Name the blood parasite species.
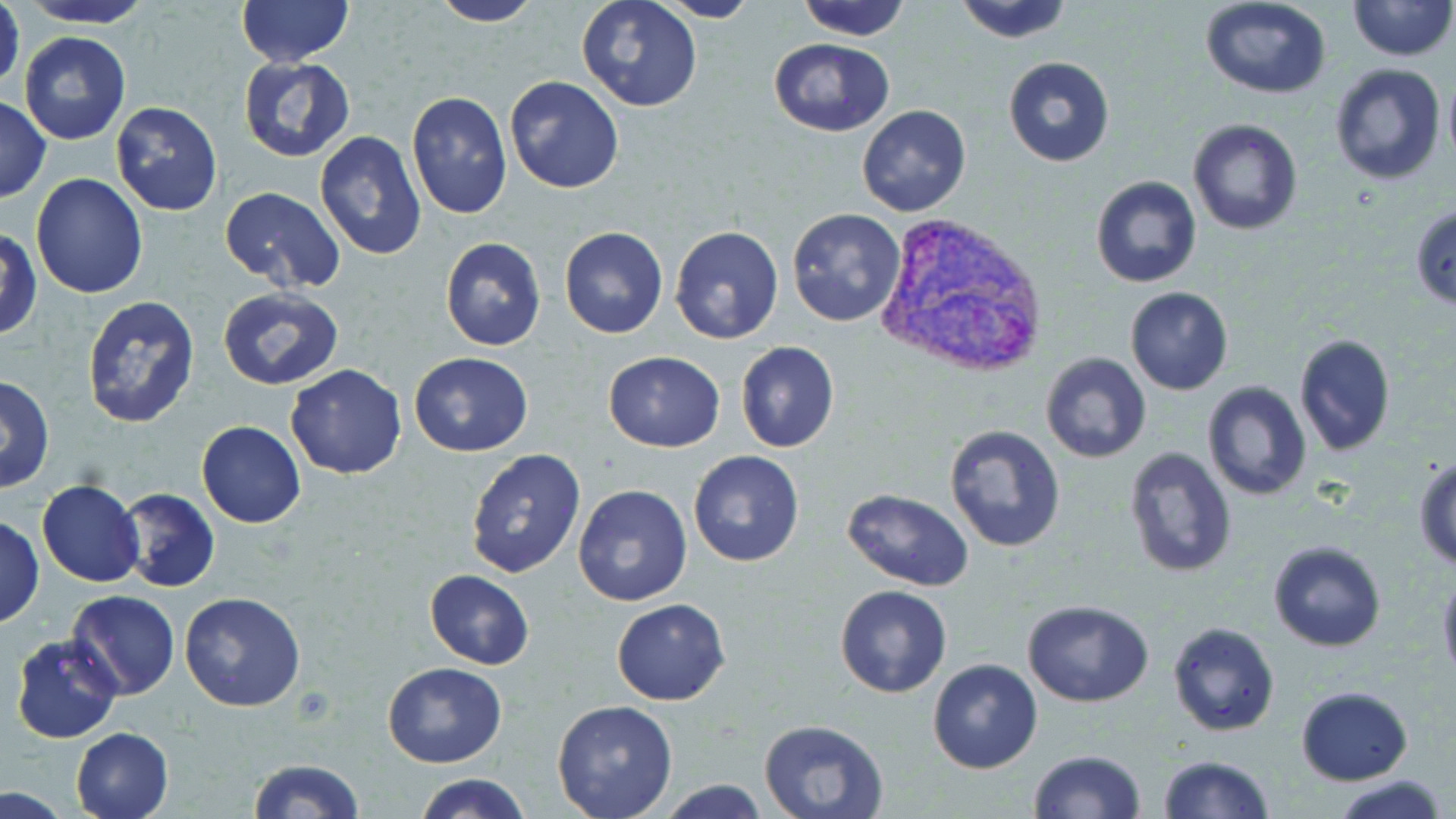
Plasmodium vivax.

Approximate bounding boxes as named x1/y1/x2/y2 corners in pixels. Uninfected red blood cell locations: (x1=18, y1=0, x2=157, y2=29), (x1=234, y1=0, x2=357, y2=67), (x1=576, y1=0, x2=704, y2=112), (x1=795, y1=0, x2=911, y2=42), (x1=952, y1=0, x2=1074, y2=44), (x1=1198, y1=0, x2=1333, y2=100), (x1=1348, y1=0, x2=1452, y2=61), (x1=1, y1=1, x2=24, y2=102), (x1=424, y1=1, x2=544, y2=27), (x1=655, y1=1, x2=762, y2=23), (x1=20, y1=31, x2=130, y2=146), (x1=768, y1=36, x2=894, y2=137), (x1=239, y1=56, x2=354, y2=162), (x1=1002, y1=57, x2=1115, y2=167), (x1=1329, y1=63, x2=1447, y2=185), (x1=1442, y1=69, x2=1456, y2=168), (x1=504, y1=74, x2=625, y2=194), (x1=406, y1=91, x2=511, y2=219), (x1=0, y1=94, x2=51, y2=203), (x1=111, y1=102, x2=222, y2=216), (x1=856, y1=104, x2=972, y2=217), (x1=1187, y1=119, x2=1303, y2=235), (x1=314, y1=131, x2=428, y2=261), (x1=31, y1=173, x2=148, y2=299), (x1=1090, y1=175, x2=1202, y2=288), (x1=218, y1=184, x2=346, y2=294), (x1=1410, y1=203, x2=1456, y2=309), (x1=787, y1=209, x2=908, y2=328), (x1=670, y1=226, x2=784, y2=344), (x1=559, y1=227, x2=668, y2=339), (x1=2, y1=230, x2=41, y2=340), (x1=440, y1=237, x2=547, y2=351), (x1=1125, y1=287, x2=1233, y2=396), (x1=219, y1=289, x2=344, y2=391), (x1=79, y1=294, x2=201, y2=431), (x1=1292, y1=333, x2=1397, y2=457), (x1=735, y1=341, x2=840, y2=453), (x1=603, y1=351, x2=725, y2=452), (x1=1040, y1=351, x2=1152, y2=464), (x1=408, y1=352, x2=533, y2=457), (x1=286, y1=364, x2=407, y2=480), (x1=0, y1=375, x2=54, y2=493), (x1=1202, y1=380, x2=1313, y2=501), (x1=196, y1=421, x2=306, y2=528), (x1=943, y1=424, x2=1068, y2=553), (x1=1123, y1=444, x2=1237, y2=578), (x1=464, y1=447, x2=586, y2=580), (x1=687, y1=450, x2=807, y2=568), (x1=1414, y1=454, x2=1456, y2=569), (x1=38, y1=479, x2=145, y2=587), (x1=573, y1=484, x2=692, y2=607), (x1=117, y1=488, x2=219, y2=594), (x1=842, y1=488, x2=974, y2=592), (x1=1, y1=515, x2=44, y2=628), (x1=1268, y1=540, x2=1388, y2=652), (x1=1436, y1=568, x2=1456, y2=687), (x1=425, y1=569, x2=534, y2=668), (x1=834, y1=584, x2=954, y2=698), (x1=65, y1=591, x2=180, y2=700), (x1=179, y1=592, x2=306, y2=711), (x1=612, y1=597, x2=731, y2=705), (x1=1022, y1=599, x2=1153, y2=707), (x1=1168, y1=622, x2=1280, y2=736), (x1=10, y1=633, x2=124, y2=745), (x1=928, y1=658, x2=1043, y2=774), (x1=382, y1=662, x2=507, y2=766), (x1=1296, y1=686, x2=1412, y2=784), (x1=551, y1=700, x2=678, y2=819), (x1=758, y1=718, x2=889, y2=818), (x1=71, y1=727, x2=175, y2=818), (x1=1029, y1=748, x2=1146, y2=819), (x1=1155, y1=755, x2=1274, y2=819), (x1=245, y1=758, x2=364, y2=819), (x1=413, y1=774, x2=532, y2=819), (x1=1337, y1=776, x2=1447, y2=819), (x1=656, y1=780, x2=773, y2=818), (x1=0, y1=787, x2=76, y2=817). Plasmodium vivax-infected red blood cell locations: (x1=875, y1=213, x2=1048, y2=379). Captured at 1000x magnification. Optical microscopy. Single field of view. Thin blood smear. May-Grünwald-Giemsa-stained preparation. Image is 1456×819 pixels.